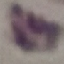

Summary:
  - Result: no malaria parasites detected
  - Stain: Giemsa
  - Capture: smartphone camera at the microscope eyepiece
  - Image type: cell patch, automatically extracted from a larger field of view and resized to 64 × 64 pixels
  - Preparation: thin blood film